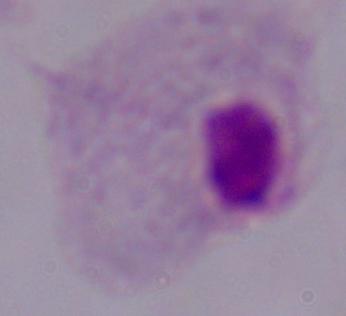
Captured at 1000x magnification. Photomicrograph. A trichomonad is seen.